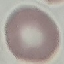

{
  "malaria_status": "uninfected",
  "capture": "smartphone through the microscope eyepiece",
  "image_type": "automatically extracted cell patch, resized to 64 × 64 pixels",
  "stain": "Giemsa",
  "preparation": "thin blood smear"
}